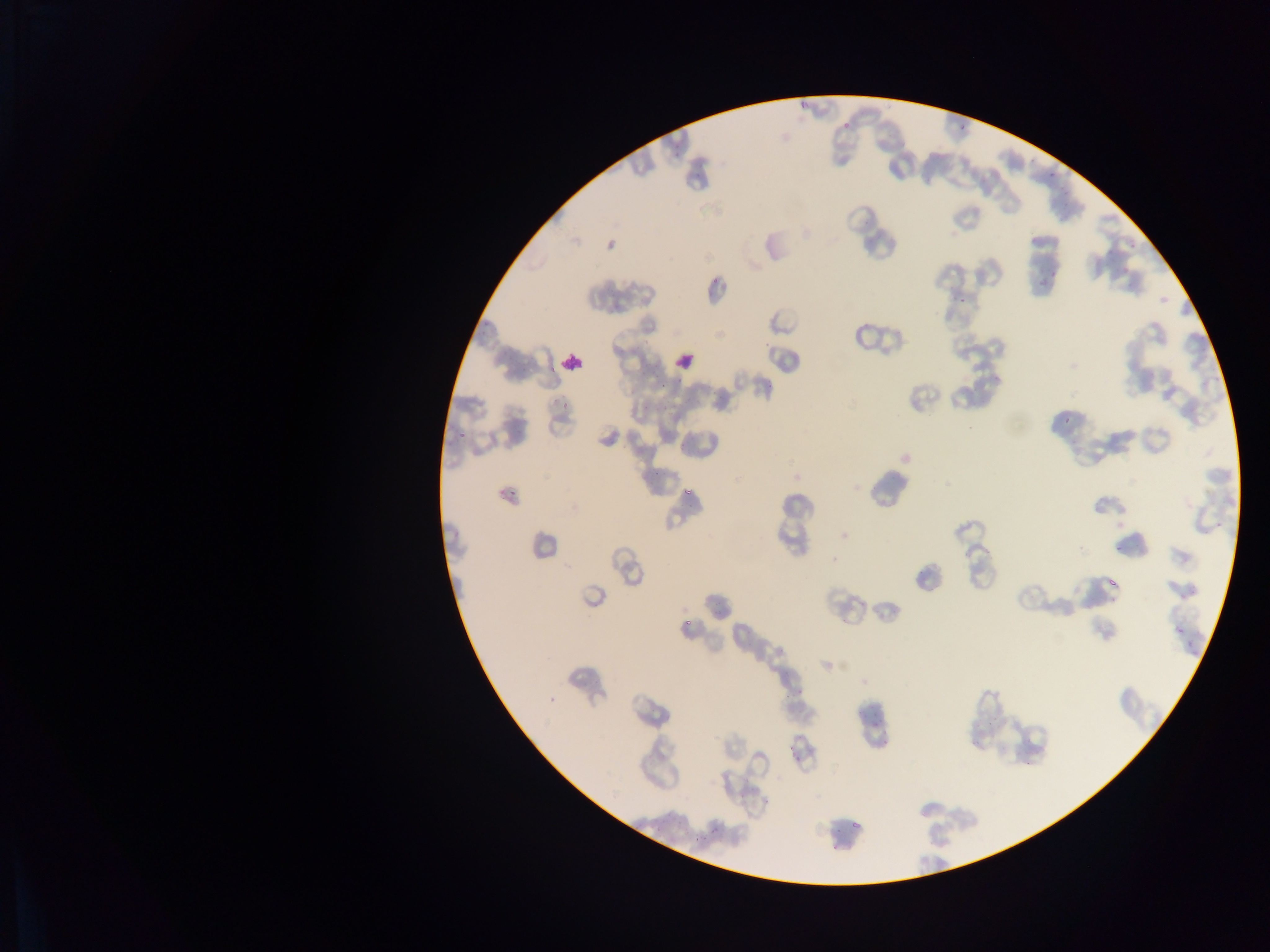
field of view = single
image size = 1270×952 pixels
country = Ghana
capture = mobile-phone photograph through a microscope
preparation = thin blood film
Plasmodium parasite locations = approximate bounding boxes as [left, top, right, bottom] in pixels: [841, 120, 853, 133], [953, 122, 970, 139], [1048, 173, 1054, 181], [1123, 234, 1138, 253], [1048, 271, 1055, 279], [956, 291, 968, 305], [1063, 413, 1071, 424], [457, 426, 468, 437], [649, 464, 664, 477], [505, 480, 516, 507], [677, 483, 694, 500], [1114, 535, 1127, 552], [1107, 567, 1126, 588], [682, 615, 695, 626], [865, 711, 875, 726], [791, 749, 809, 771], [846, 808, 862, 831]
leukocyte locations = approximate bounding boxes as [left, top, right, bottom] in pixels: [669, 346, 700, 377], [556, 347, 588, 378]